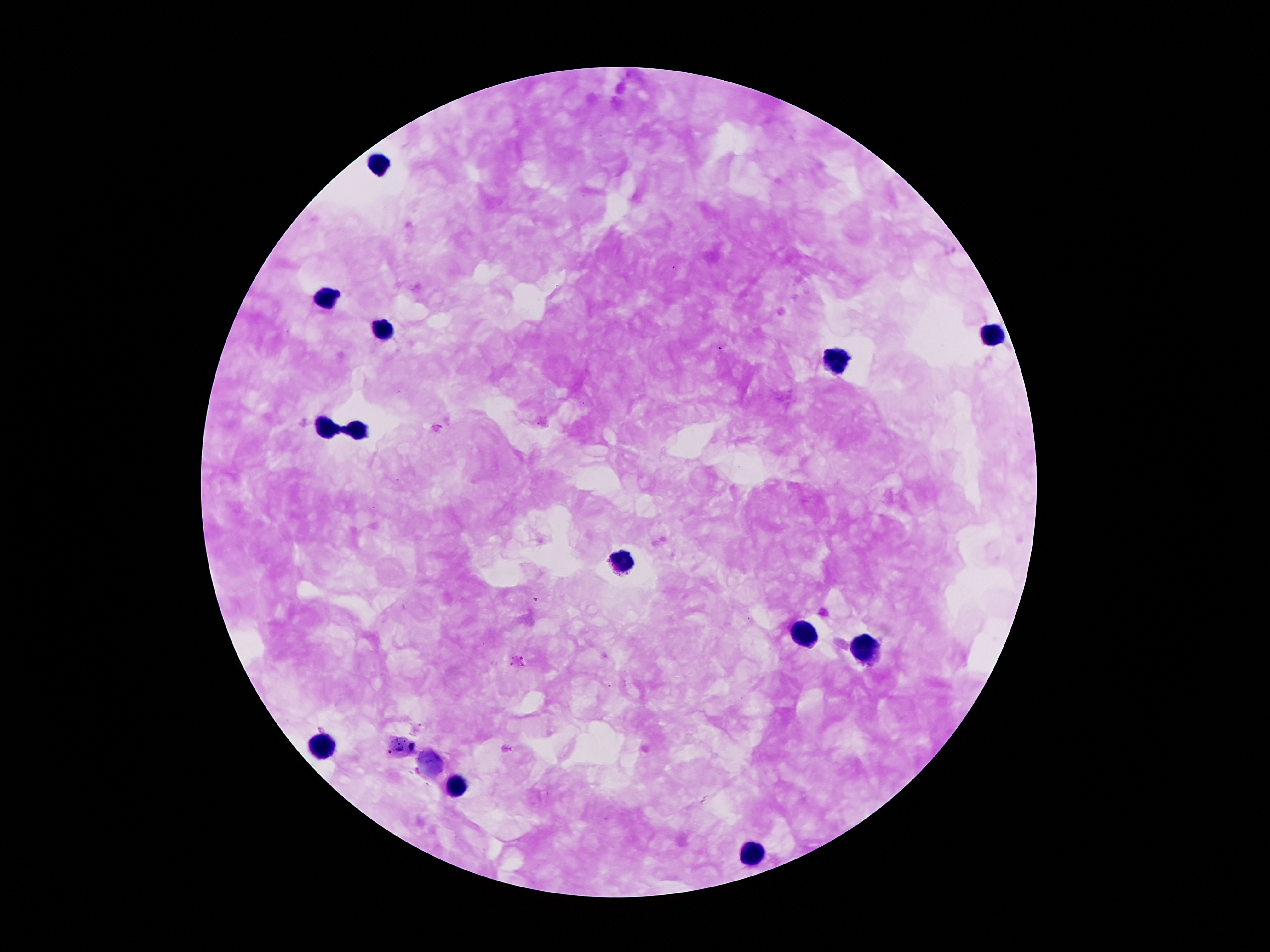

Approximate object centers, in pixels from the top-left corner.
Summary:
  - Leukocyte locations: (x=378, y=166), (x=325, y=296), (x=382, y=329), (x=989, y=336), (x=832, y=367), (x=325, y=430), (x=353, y=430), (x=619, y=565), (x=806, y=634), (x=865, y=646), (x=326, y=749), (x=451, y=789), (x=752, y=855)
  - Plasmodium parasite locations: (x=534, y=600), (x=518, y=662)
  - Image size: 1270×952 pixels
  - Preparation: thick blood film
  - Patient malaria status: positive for Plasmodium falciparum
  - Stain: Giemsa
  - Magnification: 100x
  - Field of view: single
  - Capture: smartphone camera through the microscope eyepiece